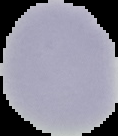
Image is 118×136 pixels. The area outside the segmented cell region is set to black. From a thin blood film. Malaria status: uninfected.